Locate every blood parasite and identify its species.
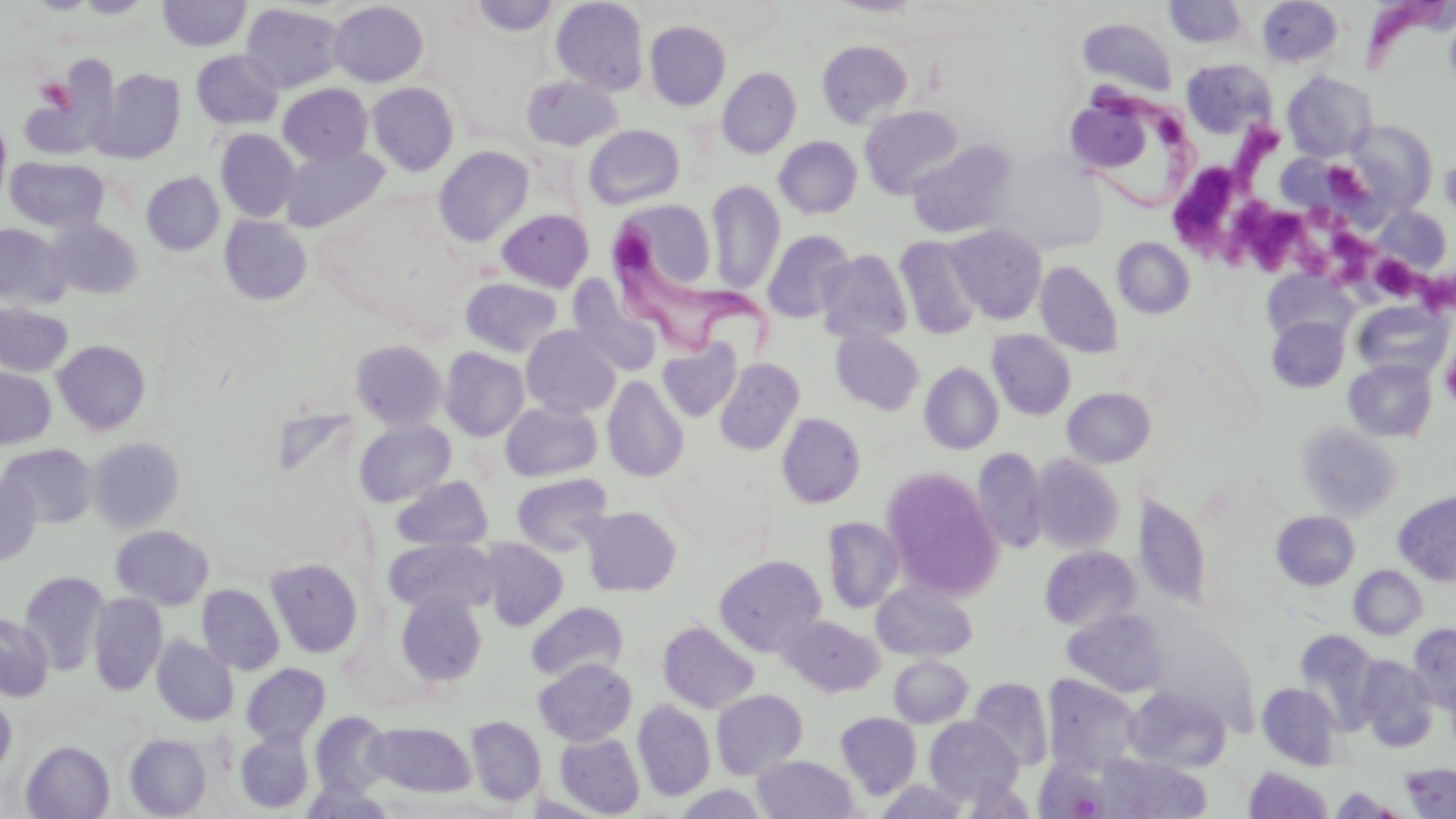
Approximate bounding boxes as [x1, y1, x2, y2] in pixels.
Trypanosoma brucei: [1363, 0, 1445, 72], [1063, 87, 1194, 207], [614, 230, 771, 363].
No Plasmodium falciparum, Plasmodium ovale, Plasmodium malariae, Plasmodium vivax, or Babesia divergens observed.

slide-level diagnosis = Trypanosoma brucei
uninfected red blood cell locations = approximate bounding boxes as [x1, y1, x2, y2] in pixels: [24, 0, 99, 14], [74, 0, 153, 18], [158, 0, 251, 51], [470, 0, 560, 38], [551, 0, 649, 95], [828, 0, 926, 16], [1256, 0, 1343, 68], [330, 1, 428, 87], [1164, 1, 1247, 47], [240, 3, 345, 93], [1078, 17, 1178, 95], [644, 21, 731, 110], [817, 40, 913, 128], [191, 50, 283, 130], [1182, 59, 1277, 138], [717, 66, 802, 158], [92, 67, 186, 163], [1283, 70, 1376, 161], [521, 76, 622, 151], [367, 82, 458, 176], [278, 83, 373, 166], [1072, 101, 1152, 174], [859, 105, 963, 199], [0, 116, 11, 206], [1342, 120, 1437, 219], [583, 125, 685, 209], [215, 129, 299, 222], [774, 136, 862, 219], [906, 141, 1018, 239], [280, 145, 389, 232], [433, 145, 534, 247], [5, 156, 108, 232], [1441, 156, 1456, 221], [141, 172, 224, 255], [706, 180, 785, 295], [609, 200, 724, 314], [1375, 206, 1453, 273], [497, 209, 594, 292], [219, 215, 313, 305], [47, 219, 142, 299], [0, 224, 68, 308], [946, 225, 1047, 324], [762, 229, 856, 323], [894, 235, 983, 340], [1112, 237, 1195, 318], [816, 249, 913, 344], [1035, 260, 1123, 358], [1264, 271, 1357, 345], [567, 277, 663, 377], [460, 278, 562, 357], [1352, 301, 1452, 380], [0, 303, 72, 377], [1267, 316, 1349, 393], [521, 325, 621, 418], [830, 329, 925, 415], [987, 330, 1076, 420], [53, 340, 151, 435], [350, 340, 447, 430], [658, 340, 742, 422], [440, 347, 529, 441], [714, 358, 805, 455], [1344, 358, 1437, 442], [919, 363, 1003, 454], [0, 367, 56, 449], [602, 375, 688, 482], [505, 384, 688, 481], [1062, 388, 1156, 467], [500, 401, 603, 482], [777, 413, 866, 508], [354, 420, 456, 507], [1296, 422, 1401, 520], [87, 437, 185, 534], [0, 444, 97, 529], [971, 447, 1047, 555], [1029, 455, 1124, 554], [881, 467, 1003, 600], [511, 472, 613, 556], [0, 473, 42, 567], [391, 476, 493, 551], [1393, 490, 1456, 586], [1134, 493, 1212, 609], [581, 506, 681, 596], [1271, 511, 1359, 590], [821, 516, 905, 613], [110, 525, 214, 610], [386, 538, 497, 615], [479, 538, 569, 630], [1040, 546, 1142, 631], [714, 554, 826, 656], [266, 558, 363, 658], [1348, 565, 1428, 640], [19, 571, 109, 674], [871, 580, 978, 662], [197, 584, 285, 675], [395, 591, 487, 687], [89, 593, 167, 695], [526, 602, 628, 682], [1062, 609, 1169, 697], [0, 613, 53, 701], [779, 615, 883, 696], [658, 620, 759, 714], [1408, 623, 1456, 713], [1295, 631, 1382, 730], [152, 636, 239, 726], [889, 654, 973, 728], [1357, 656, 1438, 751], [533, 658, 637, 745], [241, 663, 330, 746], [1042, 674, 1141, 775], [967, 677, 1053, 772], [1257, 682, 1341, 769], [1127, 686, 1231, 771], [711, 689, 808, 778], [0, 696, 16, 776], [633, 699, 715, 801], [835, 711, 922, 800], [310, 712, 392, 796], [465, 716, 546, 806], [924, 717, 1023, 805], [367, 721, 477, 798], [236, 730, 314, 814], [554, 732, 645, 817], [124, 734, 212, 818], [21, 741, 115, 819], [1098, 753, 1212, 818], [752, 754, 859, 818], [1034, 759, 1109, 819], [1401, 764, 1456, 818], [1243, 766, 1333, 818], [299, 779, 396, 819], [874, 779, 970, 819], [673, 785, 770, 818], [1329, 787, 1405, 818]
stain = May-Grünwald-Giemsa
modality = light microscopy
image size = 1456×819 pixels
platelet locations = approximate bounding boxes as [x1, y1, x2, y2] in pixels: [35, 77, 74, 110], [1228, 125, 1280, 199], [1325, 161, 1365, 198], [1173, 164, 1240, 257], [1232, 194, 1308, 270], [1329, 226, 1380, 292], [1374, 254, 1413, 308], [1409, 266, 1456, 309], [1441, 348, 1456, 408]
magnification = 1000x
field of view = single
preparation = thin blood smear